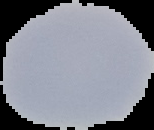
{
  "image_size": "154×130 pixels",
  "preparation": "thin blood smear",
  "image_type": "segmented cell region with the area outside set to black",
  "malaria_status": "uninfected"
}